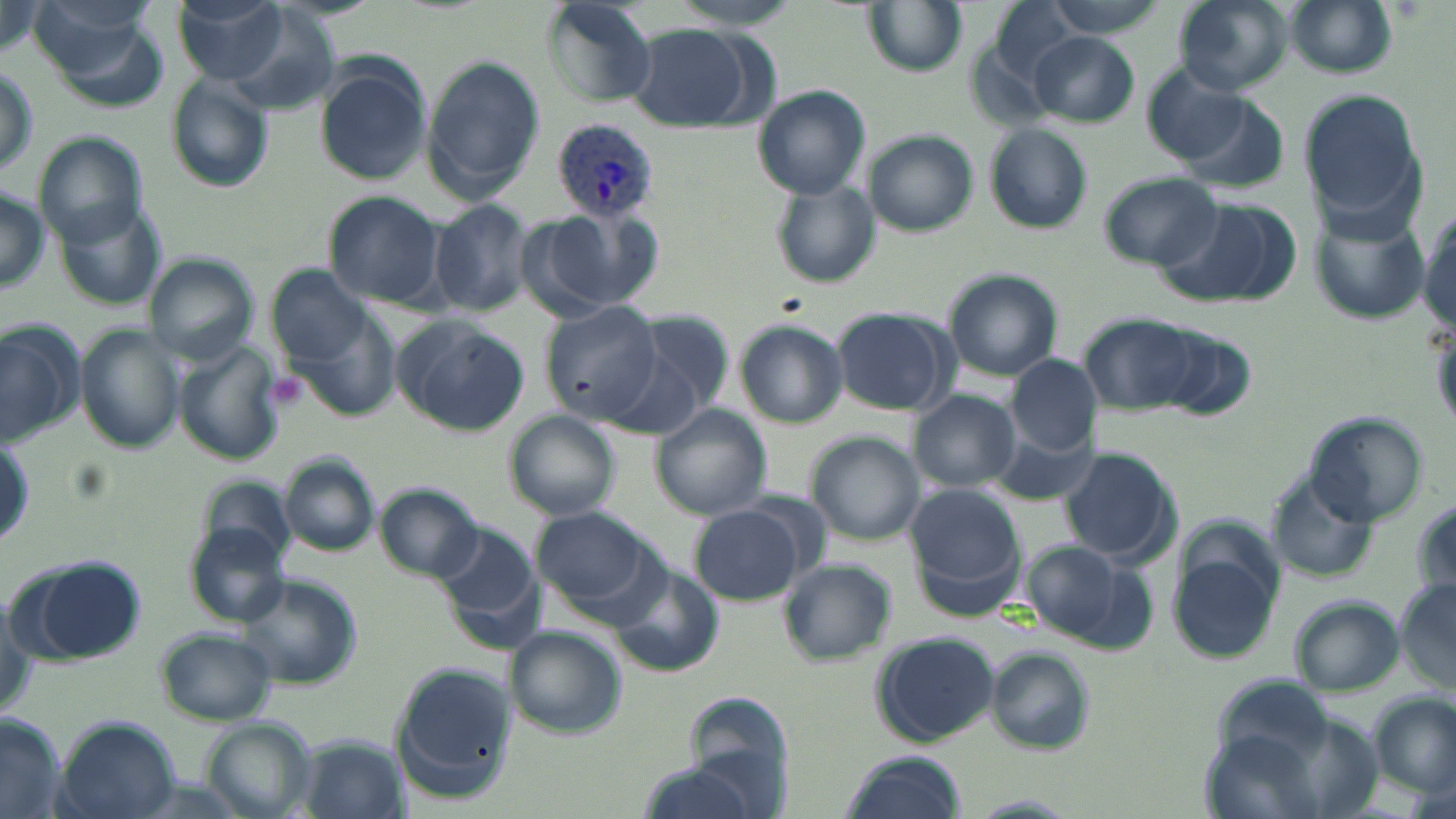

Summary:
  - Coordinate format: approximate bounding boxes as named x1/y1/x2/y2 corners in pixels
  - Plasmodium vivax-infected red blood cell locations: (x1=552, y1=119, x2=662, y2=221)
  - Uninfected red blood cell locations: (x1=171, y1=0, x2=291, y2=84), (x1=671, y1=0, x2=803, y2=29), (x1=862, y1=0, x2=968, y2=76), (x1=1042, y1=0, x2=1174, y2=37), (x1=1174, y1=0, x2=1294, y2=95), (x1=0, y1=1, x2=45, y2=56), (x1=988, y1=1, x2=1086, y2=86), (x1=1281, y1=1, x2=1396, y2=80), (x1=541, y1=3, x2=659, y2=106), (x1=223, y1=9, x2=340, y2=115), (x1=627, y1=25, x2=755, y2=130), (x1=1029, y1=32, x2=1138, y2=127), (x1=421, y1=54, x2=546, y2=197), (x1=314, y1=56, x2=431, y2=187), (x1=1, y1=59, x2=38, y2=180), (x1=1143, y1=66, x2=1252, y2=166), (x1=165, y1=76, x2=275, y2=193), (x1=753, y1=86, x2=870, y2=199), (x1=1302, y1=87, x2=1427, y2=229), (x1=1169, y1=94, x2=1292, y2=197), (x1=984, y1=124, x2=1092, y2=233), (x1=863, y1=130, x2=977, y2=237), (x1=35, y1=136, x2=147, y2=247), (x1=1097, y1=171, x2=1224, y2=270), (x1=772, y1=181, x2=881, y2=289), (x1=0, y1=184, x2=48, y2=295), (x1=324, y1=190, x2=448, y2=309), (x1=429, y1=199, x2=534, y2=317), (x1=50, y1=200, x2=166, y2=312), (x1=1312, y1=200, x2=1432, y2=327), (x1=1157, y1=202, x2=1284, y2=305), (x1=539, y1=204, x2=664, y2=317), (x1=1416, y1=210, x2=1455, y2=339), (x1=148, y1=254, x2=259, y2=364), (x1=267, y1=266, x2=372, y2=365), (x1=942, y1=269, x2=1064, y2=381), (x1=541, y1=303, x2=662, y2=422), (x1=831, y1=306, x2=957, y2=416), (x1=627, y1=310, x2=734, y2=425), (x1=293, y1=312, x2=402, y2=422), (x1=1082, y1=313, x2=1204, y2=413), (x1=394, y1=318, x2=528, y2=435), (x1=0, y1=320, x2=86, y2=445), (x1=734, y1=320, x2=847, y2=428), (x1=76, y1=325, x2=186, y2=455), (x1=1153, y1=327, x2=1256, y2=424), (x1=173, y1=339, x2=286, y2=464), (x1=1006, y1=355, x2=1103, y2=452), (x1=911, y1=392, x2=1019, y2=491), (x1=652, y1=404, x2=771, y2=520), (x1=505, y1=411, x2=622, y2=521), (x1=1304, y1=412, x2=1427, y2=525), (x1=986, y1=416, x2=1097, y2=506), (x1=806, y1=432, x2=924, y2=544), (x1=1059, y1=447, x2=1179, y2=565), (x1=278, y1=454, x2=381, y2=558), (x1=1268, y1=472, x2=1381, y2=584), (x1=906, y1=483, x2=1026, y2=606), (x1=376, y1=484, x2=481, y2=580), (x1=1413, y1=499, x2=1454, y2=600), (x1=689, y1=504, x2=808, y2=606), (x1=532, y1=507, x2=655, y2=610), (x1=428, y1=523, x2=545, y2=650), (x1=186, y1=524, x2=289, y2=628), (x1=1165, y1=538, x2=1284, y2=667), (x1=1021, y1=543, x2=1156, y2=650), (x1=16, y1=555, x2=148, y2=667), (x1=777, y1=559, x2=896, y2=666), (x1=607, y1=564, x2=725, y2=678), (x1=234, y1=574, x2=361, y2=690), (x1=1395, y1=579, x2=1456, y2=691), (x1=1289, y1=596, x2=1403, y2=699), (x1=156, y1=628, x2=276, y2=725), (x1=504, y1=629, x2=624, y2=733), (x1=871, y1=631, x2=1000, y2=746), (x1=986, y1=649, x2=1096, y2=754), (x1=391, y1=661, x2=514, y2=801), (x1=1373, y1=696, x2=1455, y2=798), (x1=662, y1=709, x2=792, y2=819), (x1=0, y1=714, x2=66, y2=818), (x1=51, y1=716, x2=181, y2=819), (x1=199, y1=718, x2=320, y2=819), (x1=294, y1=736, x2=407, y2=819), (x1=837, y1=751, x2=968, y2=819), (x1=633, y1=761, x2=768, y2=819), (x1=961, y1=795, x2=1082, y2=817)
  - Platelet locations: (x1=260, y1=370, x2=312, y2=415)
  - Slide-level diagnosis: Plasmodium vivax
  - Preparation: thin blood smear
  - Field of view: one of a larger specimen
  - Modality: light microscopy
  - Magnification: 1000x
  - Stain: May-Grünwald-Giemsa
  - Image size: 1456×819 pixels